State the blood parasite species.
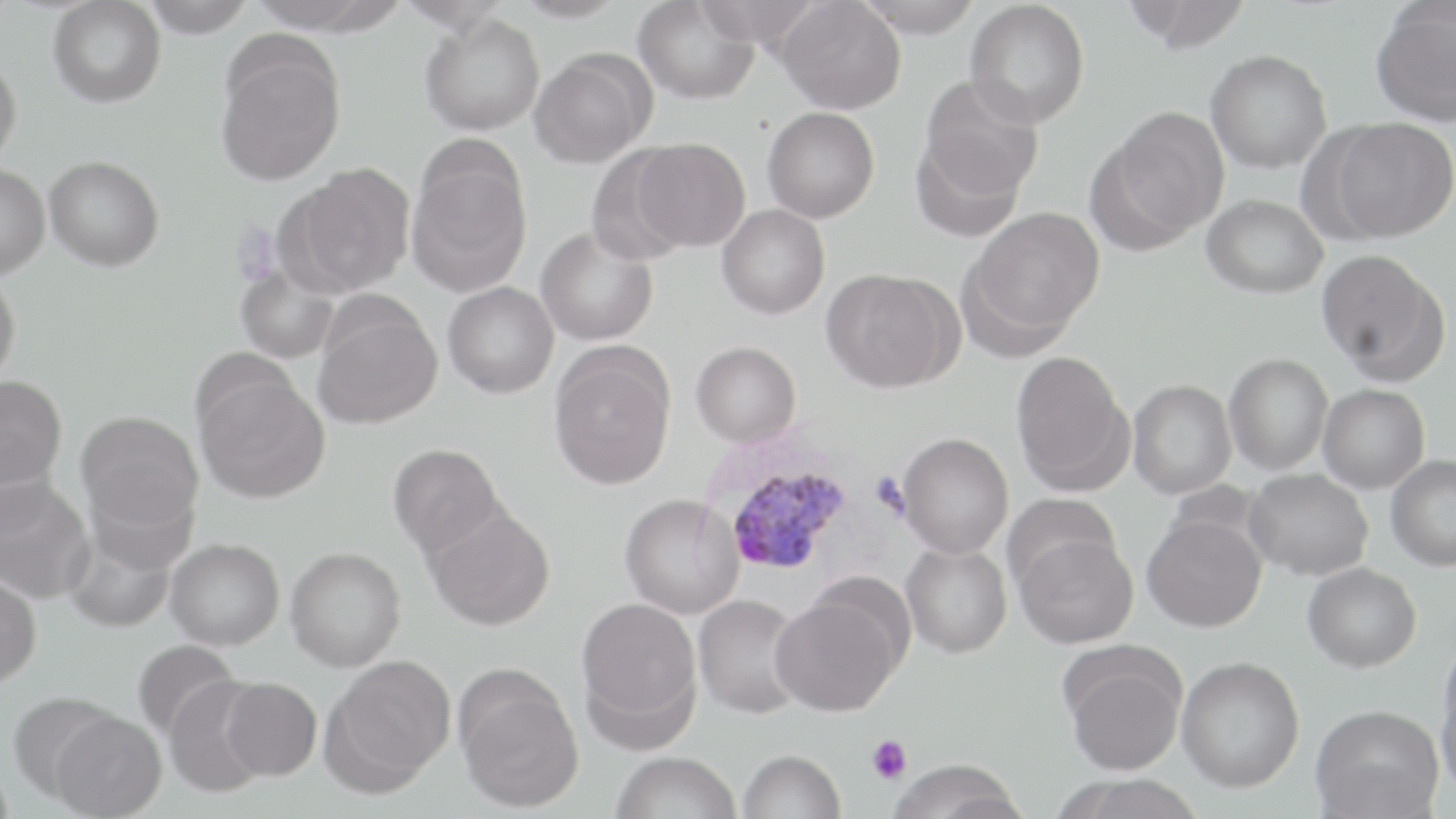

Plasmodium vivax.

Approximate bounding boxes as named x1/y1/x2/y2 corners in pixels. Platelet locations: (x1=871, y1=472, x2=908, y2=517), (x1=866, y1=735, x2=911, y2=784). Plasmodium vivax-infected red blood cell locations: (x1=713, y1=448, x2=855, y2=578). Uninfected red blood cell locations: (x1=140, y1=0, x2=257, y2=38), (x1=511, y1=0, x2=629, y2=22), (x1=633, y1=0, x2=759, y2=105), (x1=693, y1=0, x2=822, y2=48), (x1=776, y1=0, x2=906, y2=114), (x1=854, y1=0, x2=984, y2=38), (x1=1122, y1=0, x2=1253, y2=54), (x1=48, y1=1, x2=166, y2=108), (x1=965, y1=1, x2=1089, y2=128), (x1=1369, y1=3, x2=1456, y2=126), (x1=420, y1=14, x2=545, y2=136), (x1=215, y1=42, x2=347, y2=186), (x1=1205, y1=50, x2=1332, y2=173), (x1=528, y1=52, x2=651, y2=168), (x1=0, y1=56, x2=22, y2=168), (x1=919, y1=77, x2=1044, y2=205), (x1=762, y1=106, x2=880, y2=223), (x1=1102, y1=108, x2=1230, y2=242), (x1=1328, y1=118, x2=1456, y2=242), (x1=630, y1=138, x2=751, y2=252), (x1=586, y1=146, x2=695, y2=265), (x1=406, y1=150, x2=532, y2=295), (x1=44, y1=155, x2=165, y2=271), (x1=287, y1=163, x2=416, y2=296), (x1=0, y1=164, x2=50, y2=280), (x1=1201, y1=194, x2=1328, y2=299), (x1=717, y1=205, x2=830, y2=319), (x1=965, y1=206, x2=1105, y2=342), (x1=536, y1=226, x2=658, y2=347), (x1=1317, y1=250, x2=1447, y2=382), (x1=235, y1=263, x2=339, y2=364), (x1=821, y1=268, x2=958, y2=392), (x1=0, y1=269, x2=20, y2=387), (x1=443, y1=282, x2=560, y2=398), (x1=312, y1=302, x2=442, y2=429), (x1=691, y1=341, x2=801, y2=447), (x1=548, y1=344, x2=677, y2=490), (x1=1011, y1=351, x2=1131, y2=493), (x1=1224, y1=354, x2=1333, y2=475), (x1=194, y1=372, x2=330, y2=503), (x1=0, y1=375, x2=67, y2=492), (x1=1128, y1=379, x2=1236, y2=499), (x1=1318, y1=384, x2=1430, y2=494), (x1=76, y1=410, x2=204, y2=534), (x1=896, y1=432, x2=1014, y2=558), (x1=387, y1=443, x2=504, y2=557), (x1=1385, y1=454, x2=1456, y2=571), (x1=1244, y1=468, x2=1373, y2=580), (x1=0, y1=476, x2=94, y2=604), (x1=82, y1=477, x2=197, y2=576), (x1=619, y1=493, x2=744, y2=619), (x1=1004, y1=493, x2=1121, y2=593), (x1=424, y1=505, x2=556, y2=631), (x1=1142, y1=513, x2=1267, y2=632), (x1=61, y1=521, x2=180, y2=634), (x1=1015, y1=531, x2=1138, y2=649), (x1=166, y1=538, x2=284, y2=650), (x1=901, y1=542, x2=1012, y2=658), (x1=285, y1=546, x2=406, y2=671), (x1=1302, y1=562, x2=1422, y2=672), (x1=0, y1=571, x2=42, y2=688), (x1=692, y1=593, x2=807, y2=719), (x1=770, y1=593, x2=903, y2=716), (x1=576, y1=597, x2=701, y2=732), (x1=131, y1=637, x2=243, y2=743), (x1=1436, y1=649, x2=1456, y2=799), (x1=1063, y1=652, x2=1186, y2=778), (x1=326, y1=655, x2=456, y2=788), (x1=1176, y1=655, x2=1304, y2=792), (x1=455, y1=673, x2=584, y2=813), (x1=164, y1=676, x2=272, y2=797), (x1=220, y1=677, x2=322, y2=780), (x1=6, y1=690, x2=120, y2=801), (x1=1310, y1=703, x2=1444, y2=819), (x1=49, y1=710, x2=167, y2=819), (x1=739, y1=749, x2=846, y2=819), (x1=611, y1=751, x2=741, y2=819), (x1=886, y1=757, x2=1028, y2=819), (x1=1054, y1=775, x2=1208, y2=819). Light microscopy. One field of a larger specimen. Thin blood film. Image is 1456×819 pixels. May-Grünwald-Giemsa stain. 1000x magnification.